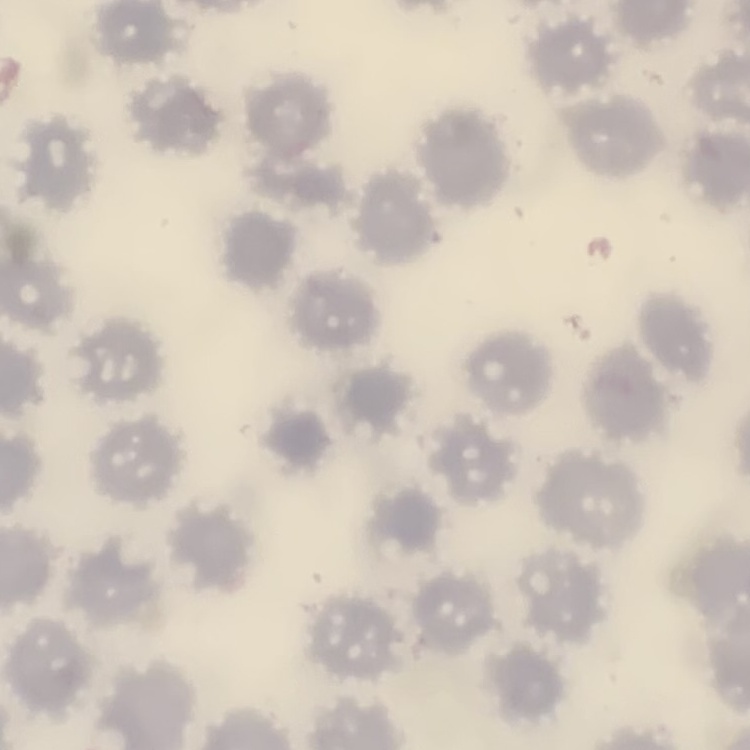
Summary:
  - Red blood cell morphology: no rouleaux formation
  - Preparation: thin peripheral smear
  - Stain: Field's or Giemsa
  - Image type: square crop of a larger photomicrograph